Describe the morphology of the red blood cells.
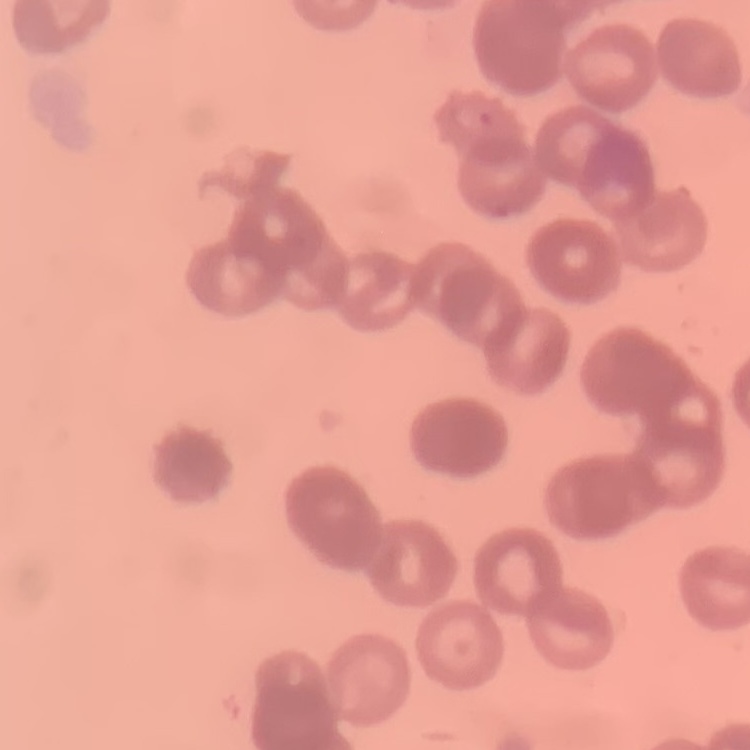

They show rouleaux formation.

{
  "image_type": "one tile cut from a larger photomicrograph",
  "preparation": "thin blood smear",
  "stain": "Field's or Giemsa"
}